Report the malaria status of this cell.
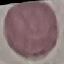

Uninfected.

capture = smartphone through the microscope eyepiece
image type = cell patch, automatically extracted from a larger field of view and resized to 64 × 64 pixels
preparation = thin blood film
stain = Giemsa